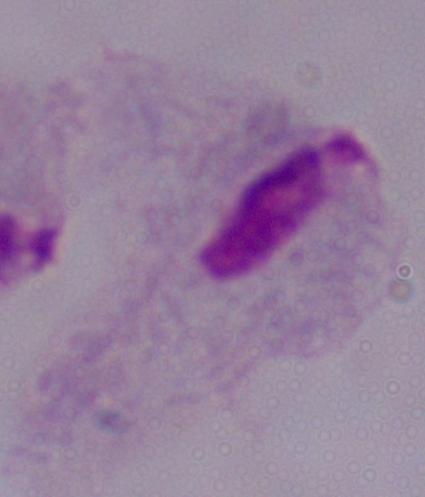
modality = micrograph
magnification = 1000x
identification = trichomonad